Describe the morphology of the red blood cells.
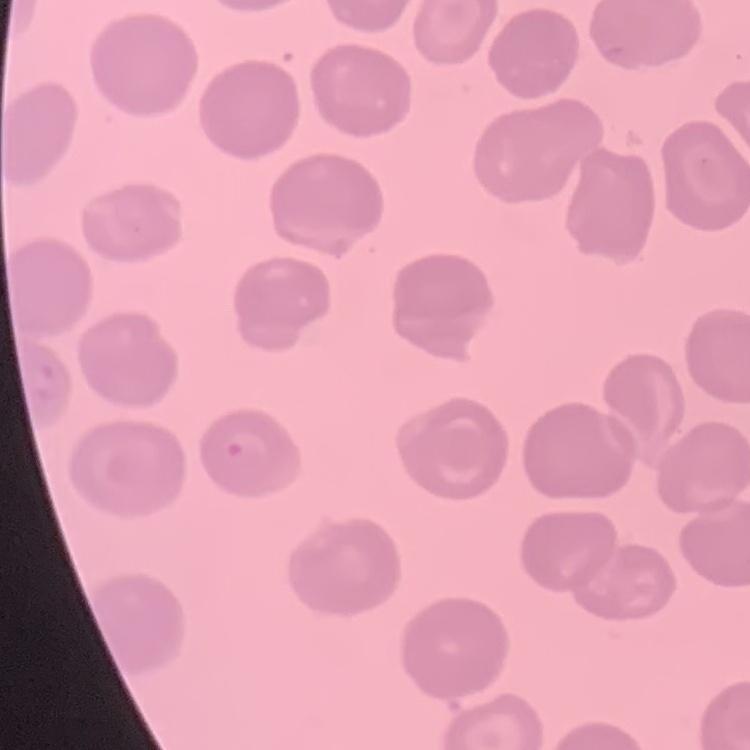
No rouleaux formation.

Summary:
  - Stain: Field's or Giemsa
  - Image type: square crop of a larger photomicrograph
  - Preparation: thin blood smear